Identify the blood parasite species.
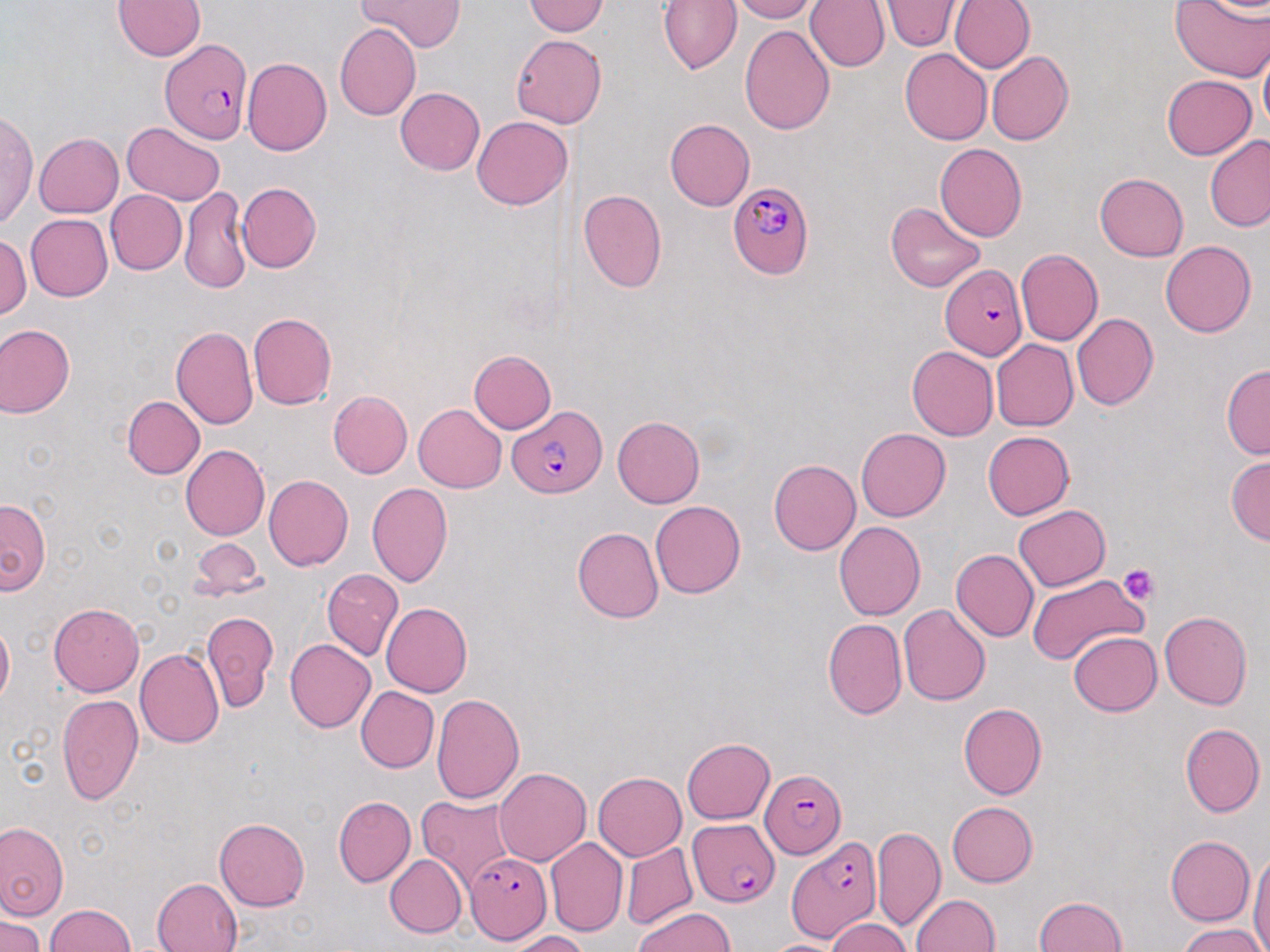

Plasmodium falciparum.

Approximate bounding boxes as named x1/y1/x2/y2 corners in pixels. Plasmodium falciparum-infected red blood cell locations: (x1=161, y1=37, x2=251, y2=143), (x1=727, y1=182, x2=814, y2=280), (x1=940, y1=264, x2=1028, y2=360), (x1=509, y1=406, x2=604, y2=500), (x1=759, y1=770, x2=844, y2=859), (x1=689, y1=819, x2=780, y2=907), (x1=786, y1=836, x2=881, y2=940), (x1=465, y1=851, x2=553, y2=942). Uninfected red blood cell locations: (x1=113, y1=0, x2=205, y2=60), (x1=355, y1=0, x2=464, y2=52), (x1=659, y1=0, x2=742, y2=74), (x1=726, y1=0, x2=816, y2=22), (x1=804, y1=0, x2=889, y2=72), (x1=880, y1=0, x2=965, y2=52), (x1=949, y1=0, x2=1035, y2=73), (x1=1169, y1=0, x2=1268, y2=82), (x1=1194, y1=0, x2=1270, y2=18), (x1=523, y1=1, x2=610, y2=36), (x1=334, y1=23, x2=420, y2=120), (x1=739, y1=25, x2=835, y2=135), (x1=511, y1=34, x2=606, y2=130), (x1=1259, y1=45, x2=1270, y2=140), (x1=900, y1=48, x2=993, y2=146), (x1=987, y1=51, x2=1073, y2=146), (x1=244, y1=58, x2=332, y2=155), (x1=1161, y1=75, x2=1256, y2=159), (x1=395, y1=86, x2=485, y2=176), (x1=1, y1=109, x2=38, y2=231), (x1=472, y1=115, x2=573, y2=210), (x1=665, y1=119, x2=754, y2=211), (x1=122, y1=122, x2=225, y2=205), (x1=35, y1=133, x2=123, y2=217), (x1=1204, y1=134, x2=1270, y2=232), (x1=935, y1=144, x2=1027, y2=242), (x1=1094, y1=173, x2=1188, y2=261), (x1=237, y1=182, x2=322, y2=273), (x1=180, y1=185, x2=251, y2=296), (x1=577, y1=188, x2=667, y2=294), (x1=105, y1=190, x2=187, y2=275), (x1=885, y1=202, x2=988, y2=293), (x1=25, y1=214, x2=112, y2=302), (x1=0, y1=233, x2=31, y2=321), (x1=1160, y1=240, x2=1256, y2=338), (x1=1015, y1=249, x2=1103, y2=345), (x1=1072, y1=312, x2=1158, y2=410), (x1=248, y1=313, x2=336, y2=410), (x1=0, y1=325, x2=75, y2=417), (x1=171, y1=327, x2=258, y2=429), (x1=991, y1=339, x2=1078, y2=432), (x1=907, y1=345, x2=998, y2=440), (x1=468, y1=350, x2=556, y2=433), (x1=1221, y1=364, x2=1270, y2=459), (x1=328, y1=391, x2=412, y2=478), (x1=122, y1=396, x2=204, y2=478), (x1=413, y1=403, x2=506, y2=493), (x1=612, y1=414, x2=705, y2=508), (x1=856, y1=429, x2=951, y2=521), (x1=983, y1=432, x2=1074, y2=519), (x1=180, y1=443, x2=269, y2=541), (x1=1227, y1=455, x2=1270, y2=545), (x1=768, y1=458, x2=861, y2=555), (x1=264, y1=474, x2=353, y2=570), (x1=366, y1=482, x2=452, y2=588), (x1=1, y1=498, x2=51, y2=594), (x1=651, y1=501, x2=744, y2=599), (x1=1012, y1=503, x2=1110, y2=591), (x1=834, y1=521, x2=925, y2=621), (x1=572, y1=527, x2=665, y2=623), (x1=189, y1=540, x2=265, y2=598), (x1=951, y1=549, x2=1039, y2=641), (x1=321, y1=569, x2=402, y2=661), (x1=1025, y1=573, x2=1149, y2=669), (x1=380, y1=602, x2=473, y2=697), (x1=49, y1=603, x2=144, y2=696), (x1=898, y1=604, x2=992, y2=706), (x1=201, y1=611, x2=277, y2=712), (x1=1159, y1=612, x2=1252, y2=710), (x1=0, y1=618, x2=13, y2=709), (x1=822, y1=618, x2=906, y2=720), (x1=1068, y1=631, x2=1162, y2=716), (x1=285, y1=639, x2=376, y2=733), (x1=135, y1=648, x2=224, y2=750), (x1=356, y1=686, x2=439, y2=772), (x1=432, y1=692, x2=526, y2=804), (x1=57, y1=694, x2=143, y2=804), (x1=958, y1=702, x2=1047, y2=800), (x1=1179, y1=723, x2=1264, y2=818), (x1=682, y1=738, x2=773, y2=824), (x1=494, y1=768, x2=591, y2=866), (x1=592, y1=772, x2=686, y2=861), (x1=334, y1=795, x2=415, y2=887), (x1=417, y1=797, x2=517, y2=890), (x1=947, y1=801, x2=1037, y2=886), (x1=214, y1=816, x2=310, y2=912), (x1=0, y1=822, x2=68, y2=920), (x1=872, y1=825, x2=944, y2=930), (x1=1165, y1=836, x2=1255, y2=925), (x1=544, y1=837, x2=628, y2=937), (x1=621, y1=841, x2=697, y2=930), (x1=1248, y1=849, x2=1270, y2=952), (x1=385, y1=854, x2=466, y2=937), (x1=152, y1=877, x2=242, y2=952), (x1=909, y1=894, x2=1000, y2=952), (x1=1034, y1=895, x2=1126, y2=951), (x1=47, y1=904, x2=135, y2=952), (x1=636, y1=907, x2=737, y2=952), (x1=2, y1=915, x2=43, y2=950), (x1=825, y1=918, x2=910, y2=951), (x1=1177, y1=924, x2=1267, y2=952), (x1=510, y1=931, x2=588, y2=952), (x1=763, y1=939, x2=844, y2=952). Platelet locations: (x1=1119, y1=564, x2=1161, y2=604). Single field of view. Thin blood film. 1000x magnification. Optical microscopy. May-Grünwald-Giemsa stain. Image is 1270×952 pixels.